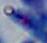
Summary:
  - Identification: Toxoplasma gondii
  - Modality: photomicrograph
  - Magnification: 1000x